Point out each leukocyte.
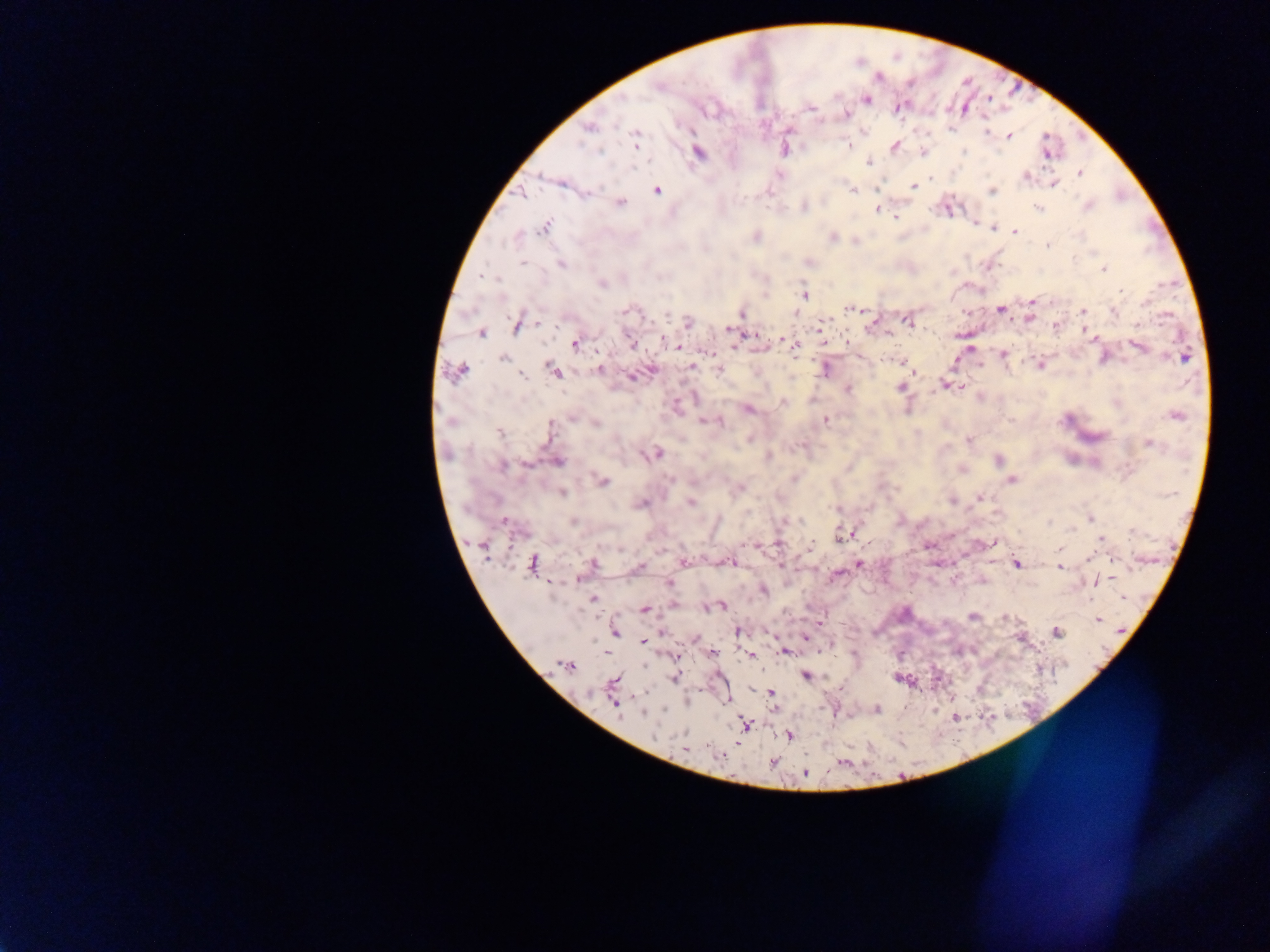
No leukocytes observed.

Approximate centers as (x, y) in pixels. Malaria parasite locations: (658, 86), (623, 99), (867, 100), (898, 108), (845, 114), (589, 129), (986, 132), (1009, 136), (635, 139), (848, 144), (895, 146), (599, 150), (964, 151), (699, 152), (923, 152), (1046, 153), (868, 162), (1079, 173), (779, 175), (1026, 176), (1053, 184), (914, 186), (656, 190), (854, 191), (992, 191), (521, 194), (621, 202), (805, 206), (1089, 206), (1038, 208), (876, 210), (947, 210), (895, 216), (974, 223), (545, 227), (994, 228), (1015, 231), (756, 237), (832, 237), (1048, 246), (524, 262), (561, 263), (809, 263), (1103, 269), (481, 277), (491, 278), (602, 284), (1122, 291), (804, 294), (1031, 301), (851, 309), (628, 310), (1001, 310), (1083, 311), (1113, 311), (741, 314), (666, 316), (1029, 318), (907, 321), (822, 322), (874, 322), (688, 323), (538, 324), (517, 326), (1055, 326), (728, 330), (480, 333), (754, 335), (1090, 335), (782, 339), (1094, 339), (664, 340), (824, 341), (575, 344), (632, 344), (676, 346), (1138, 346), (736, 347), (794, 347), (971, 347), (709, 352), (1003, 355), (504, 358), (1183, 358), (901, 362), (1040, 365), (692, 366), (599, 369), (718, 370), (826, 370), (458, 371), (554, 371), (523, 376), (632, 376), (946, 384), (900, 387), (848, 389), (782, 403), (748, 410), (1176, 417), (826, 420), (451, 421), (704, 421), (714, 421), (596, 423), (550, 425), (499, 432), (968, 440), (1148, 445), (654, 453), (998, 461), (557, 462), (526, 464), (501, 466), (962, 469), (795, 478), (1013, 480), (603, 481), (741, 488), (562, 493), (981, 497), (953, 501), (691, 503), (642, 504), (835, 509), (1090, 518), (504, 521), (573, 522), (1050, 523), (1132, 532), (841, 536), (1100, 539), (991, 543), (778, 544), (809, 547), (1059, 548), (1090, 556), (1113, 559), (684, 562), (731, 563), (532, 564), (593, 564), (859, 564), (1017, 564), (1060, 567), (638, 568), (835, 576), (578, 579), (1095, 582), (669, 584), (764, 590), (1123, 597), (593, 599), (674, 605), (721, 606), (709, 607), (645, 609), (972, 616), (1004, 618), (1098, 619), (738, 631), (615, 633), (1057, 633), (806, 637), (643, 641), (783, 651), (713, 652), (750, 655), (565, 666), (806, 675), (674, 679), (615, 681), (643, 693), (771, 694), (615, 705), (878, 709), (644, 714), (745, 725), (789, 736), (685, 748), (722, 755), (774, 762), (805, 773). Image is 1270×952 pixels. Photographed through a microscope with a mobile-phone camera. Collected in Ghana. Thick blood film. Single field of view.